Identify the cell.
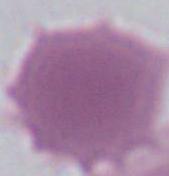
An erythrocyte.

{
  "modality": "photomicrograph",
  "magnification": "1000x"
}